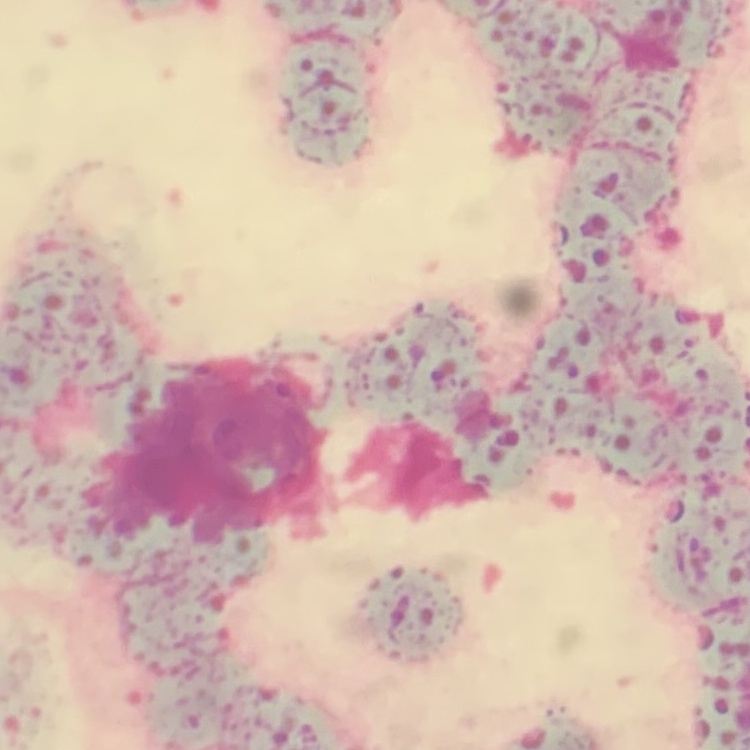

erythrocyte morphology = rouleaux formation
image type = square crop of a larger photomicrograph
preparation = thin blood smear
stain = Field's or Giemsa